Describe the morphology of the red blood cells.
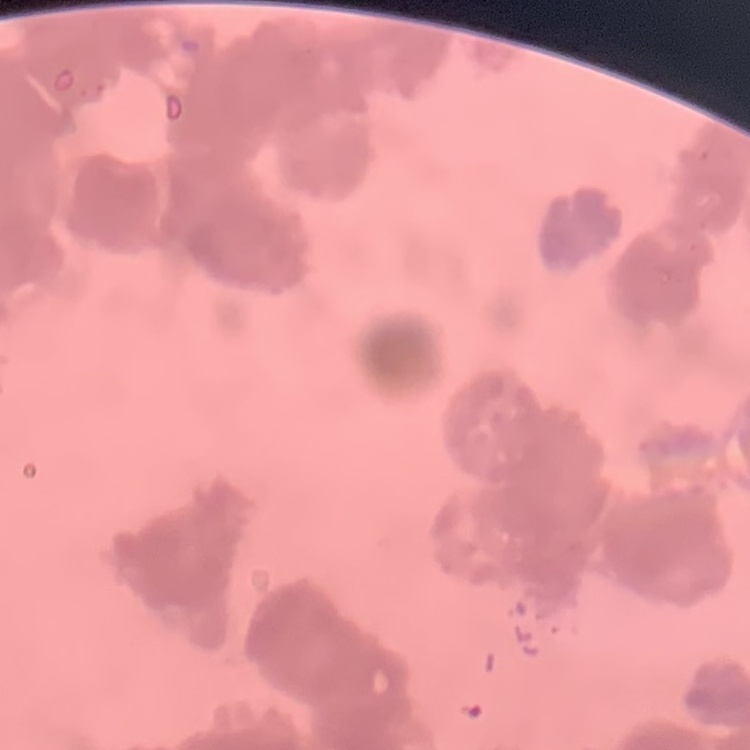

Rouleaux formation.

Square crop of a larger photomicrograph. Thin blood film. Field's or Giemsa stain.